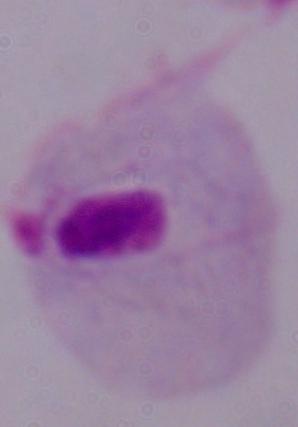
identification = trichomonad
modality = micrograph
magnification = 1000x